Assess the morphology of the red blood cells.
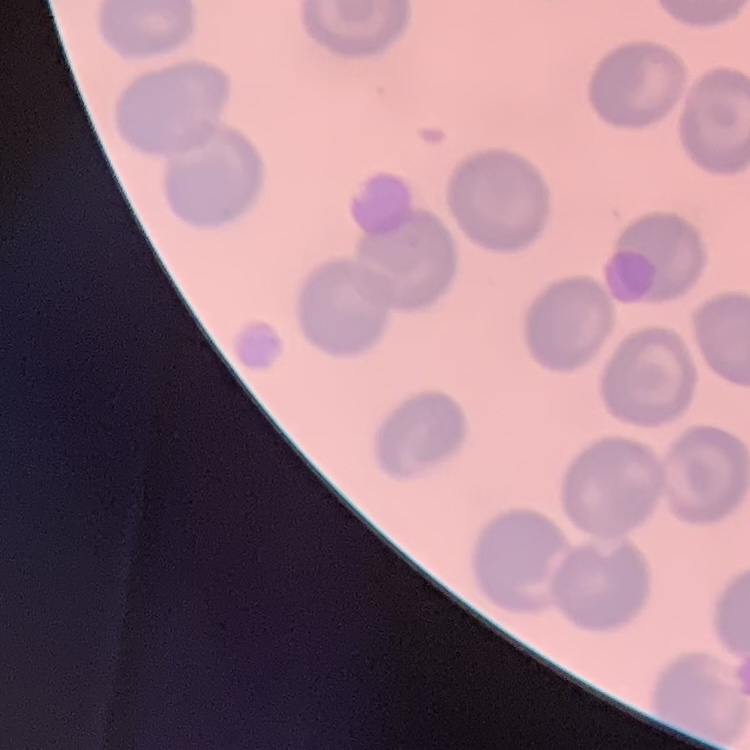
No rouleaux formation.

stain = Field's or Giemsa
preparation = thin peripheral smear
image type = one tile cut from a larger photomicrograph